Locate and identify every blood parasite.
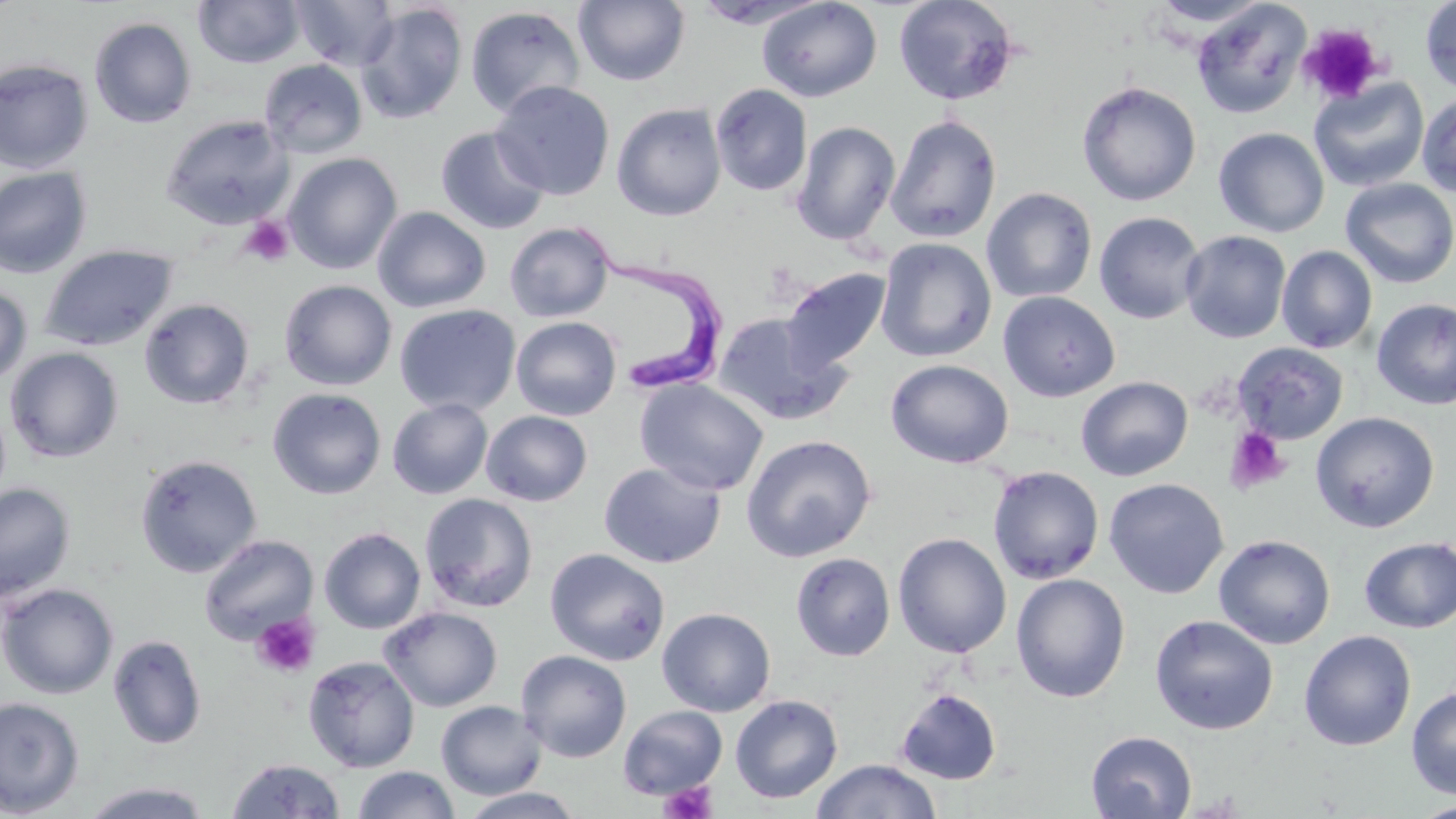

Approximate bounding boxes as named x1/y1/x2/y2 corners in pixels.
Trypanosoma brucei: (x1=572, y1=222, x2=727, y2=395).
No Plasmodium falciparum, Plasmodium ovale, Plasmodium malariae, Plasmodium vivax, or Babesia divergens observed.

Uninfected red blood cell locations: (x1=193, y1=0, x2=304, y2=68), (x1=291, y1=0, x2=400, y2=72), (x1=572, y1=0, x2=691, y2=86), (x1=757, y1=0, x2=882, y2=102), (x1=893, y1=0, x2=1019, y2=106), (x1=1148, y1=0, x2=1272, y2=28), (x1=1420, y1=0, x2=1456, y2=95), (x1=1191, y1=2, x2=1312, y2=119), (x1=355, y1=3, x2=469, y2=125), (x1=466, y1=6, x2=585, y2=118), (x1=89, y1=17, x2=197, y2=128), (x1=0, y1=59, x2=94, y2=174), (x1=258, y1=59, x2=368, y2=158), (x1=1309, y1=76, x2=1430, y2=193), (x1=490, y1=80, x2=615, y2=200), (x1=1076, y1=81, x2=1202, y2=206), (x1=710, y1=84, x2=813, y2=196), (x1=1416, y1=92, x2=1456, y2=198), (x1=612, y1=103, x2=727, y2=221), (x1=160, y1=114, x2=294, y2=230), (x1=885, y1=114, x2=1002, y2=243), (x1=791, y1=121, x2=901, y2=246), (x1=435, y1=126, x2=550, y2=235), (x1=1213, y1=127, x2=1329, y2=238), (x1=283, y1=152, x2=402, y2=274), (x1=0, y1=166, x2=92, y2=279), (x1=1340, y1=178, x2=1456, y2=288), (x1=981, y1=187, x2=1097, y2=303), (x1=372, y1=206, x2=492, y2=313), (x1=1093, y1=211, x2=1207, y2=325), (x1=504, y1=221, x2=615, y2=322), (x1=1180, y1=230, x2=1291, y2=343), (x1=875, y1=238, x2=996, y2=362), (x1=39, y1=244, x2=177, y2=351), (x1=1276, y1=245, x2=1378, y2=354), (x1=781, y1=267, x2=892, y2=372), (x1=279, y1=279, x2=397, y2=391), (x1=0, y1=284, x2=32, y2=388), (x1=997, y1=291, x2=1120, y2=402), (x1=1371, y1=297, x2=1456, y2=410), (x1=139, y1=298, x2=255, y2=409), (x1=394, y1=304, x2=521, y2=417), (x1=712, y1=312, x2=852, y2=426), (x1=511, y1=317, x2=622, y2=420), (x1=1232, y1=343, x2=1349, y2=445), (x1=4, y1=347, x2=124, y2=463), (x1=884, y1=359, x2=1014, y2=469), (x1=1075, y1=376, x2=1194, y2=481), (x1=634, y1=378, x2=769, y2=496), (x1=267, y1=388, x2=386, y2=499), (x1=387, y1=398, x2=494, y2=499), (x1=481, y1=410, x2=592, y2=506), (x1=1310, y1=411, x2=1440, y2=533), (x1=741, y1=434, x2=877, y2=562), (x1=134, y1=454, x2=262, y2=577), (x1=599, y1=462, x2=726, y2=568), (x1=987, y1=465, x2=1105, y2=585), (x1=1104, y1=477, x2=1229, y2=599), (x1=0, y1=482, x2=76, y2=603), (x1=419, y1=492, x2=539, y2=613), (x1=318, y1=527, x2=426, y2=634), (x1=892, y1=532, x2=1012, y2=658), (x1=198, y1=534, x2=319, y2=646), (x1=1213, y1=534, x2=1336, y2=649), (x1=1358, y1=537, x2=1456, y2=633), (x1=545, y1=547, x2=670, y2=666), (x1=790, y1=552, x2=895, y2=661), (x1=1010, y1=573, x2=1130, y2=703), (x1=0, y1=583, x2=119, y2=700), (x1=379, y1=606, x2=502, y2=712), (x1=657, y1=607, x2=776, y2=716), (x1=1149, y1=614, x2=1279, y2=735), (x1=1299, y1=630, x2=1417, y2=750), (x1=108, y1=633, x2=206, y2=750), (x1=516, y1=650, x2=632, y2=762), (x1=302, y1=655, x2=420, y2=772), (x1=1406, y1=686, x2=1456, y2=799), (x1=895, y1=687, x2=1002, y2=785), (x1=730, y1=695, x2=843, y2=803), (x1=0, y1=697, x2=84, y2=817), (x1=436, y1=700, x2=546, y2=800), (x1=617, y1=705, x2=728, y2=801), (x1=1086, y1=731, x2=1197, y2=818), (x1=226, y1=758, x2=347, y2=817), (x1=810, y1=759, x2=943, y2=819), (x1=352, y1=766, x2=460, y2=819), (x1=82, y1=781, x2=211, y2=818), (x1=455, y1=787, x2=588, y2=818), (x1=1413, y1=801, x2=1456, y2=819). Platelet locations: (x1=1297, y1=24, x2=1385, y2=106), (x1=238, y1=216, x2=294, y2=267), (x1=1225, y1=427, x2=1291, y2=495), (x1=252, y1=614, x2=320, y2=678), (x1=658, y1=780, x2=718, y2=819). Slide-level diagnosis: Trypanosoma brucei. Image is 1456×819 pixels. Thin blood smear. May-Grünwald-Giemsa stain. Single field of view. Captured at 1000x magnification. Optical microscopy.